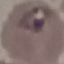
Summary:
  - Result: malaria parasites identified
  - Preparation: thin blood film
  - Capture: smartphone through the microscope eyepiece
  - Stain: Giemsa
  - Image type: automatically extracted cell patch, resized to 64 × 64 pixels